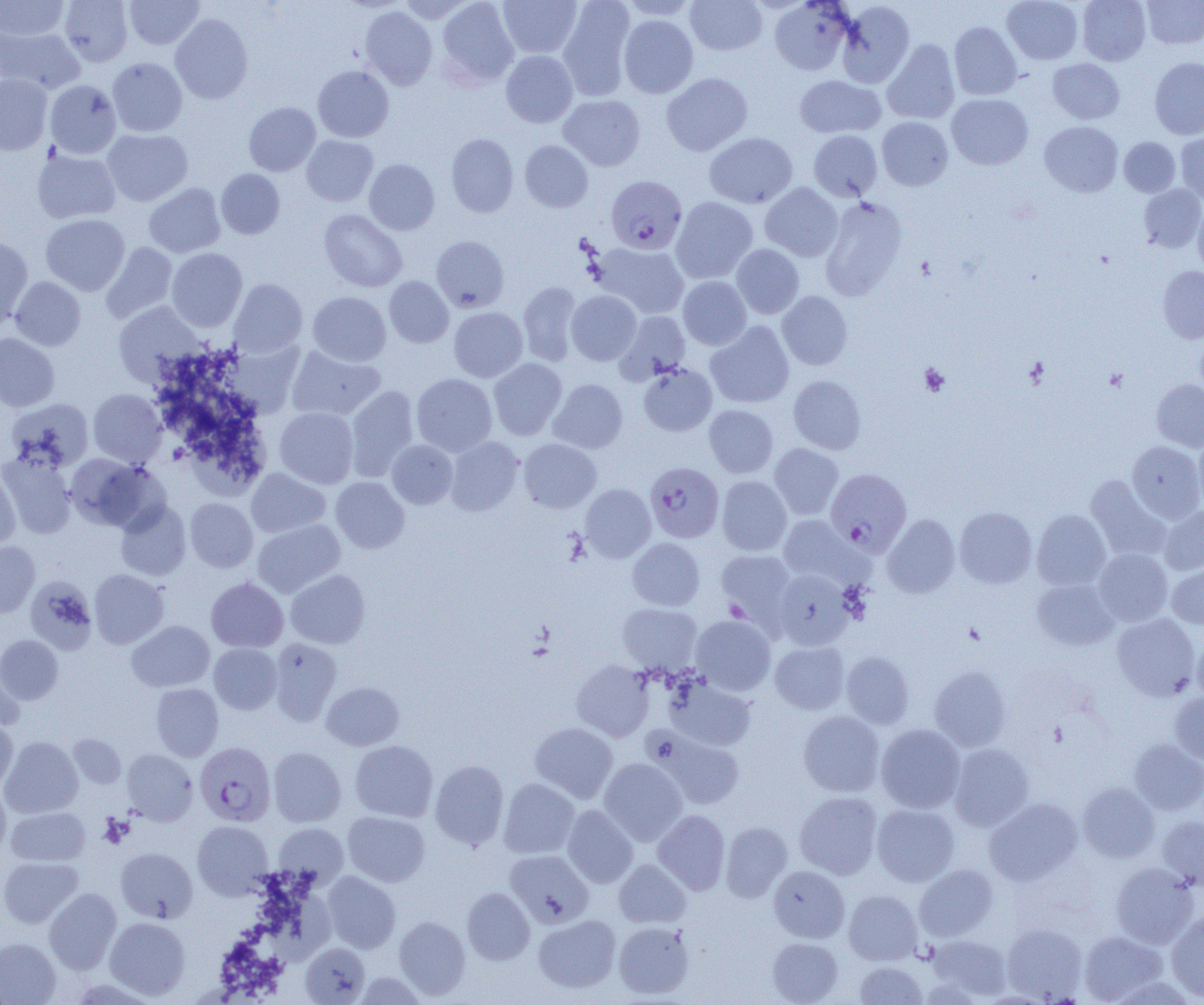

Approximate bounding boxes as named x1/y1/x2/y2 corners in pixels. Platelet locations: (x1=919, y1=363, x2=950, y2=396), (x1=99, y1=815, x2=133, y2=847). Plasmodium falciparum-infected red blood cell locations (subset): (x1=645, y1=461, x2=724, y2=543), (x1=826, y1=469, x2=911, y2=555), (x1=195, y1=742, x2=276, y2=826). Uninfected red blood cell locations (subset): (x1=0, y1=0, x2=69, y2=40), (x1=59, y1=0, x2=133, y2=66), (x1=125, y1=0, x2=204, y2=49), (x1=436, y1=0, x2=518, y2=88), (x1=498, y1=0, x2=582, y2=58), (x1=685, y1=0, x2=767, y2=55), (x1=1002, y1=0, x2=1083, y2=65), (x1=1078, y1=0, x2=1151, y2=65), (x1=1141, y1=0, x2=1204, y2=49), (x1=557, y1=1, x2=636, y2=100), (x1=619, y1=1, x2=699, y2=21), (x1=769, y1=1, x2=853, y2=75), (x1=836, y1=1, x2=915, y2=88), (x1=360, y1=6, x2=437, y2=90), (x1=170, y1=14, x2=253, y2=104), (x1=619, y1=15, x2=698, y2=98), (x1=949, y1=21, x2=1021, y2=100), (x1=0, y1=27, x2=85, y2=93), (x1=882, y1=39, x2=960, y2=125), (x1=501, y1=50, x2=578, y2=128), (x1=107, y1=58, x2=187, y2=136), (x1=1048, y1=58, x2=1125, y2=124), (x1=1149, y1=58, x2=1204, y2=139), (x1=312, y1=65, x2=394, y2=143), (x1=661, y1=73, x2=752, y2=156), (x1=0, y1=75, x2=52, y2=155), (x1=795, y1=75, x2=885, y2=138), (x1=45, y1=80, x2=121, y2=159), (x1=946, y1=93, x2=1033, y2=169), (x1=559, y1=94, x2=645, y2=171), (x1=244, y1=102, x2=321, y2=176), (x1=877, y1=116, x2=953, y2=190), (x1=1040, y1=121, x2=1123, y2=197), (x1=102, y1=129, x2=193, y2=206), (x1=808, y1=130, x2=883, y2=201), (x1=704, y1=132, x2=797, y2=208), (x1=446, y1=133, x2=518, y2=217), (x1=1176, y1=134, x2=1203, y2=203), (x1=301, y1=135, x2=378, y2=206), (x1=1119, y1=137, x2=1180, y2=197), (x1=520, y1=140, x2=593, y2=212), (x1=32, y1=148, x2=121, y2=224), (x1=364, y1=159, x2=439, y2=234), (x1=216, y1=168, x2=285, y2=239), (x1=144, y1=183, x2=225, y2=257), (x1=760, y1=183, x2=843, y2=261), (x1=1138, y1=184, x2=1204, y2=253), (x1=671, y1=197, x2=758, y2=283), (x1=820, y1=197, x2=907, y2=299), (x1=1193, y1=202, x2=1204, y2=275), (x1=319, y1=209, x2=407, y2=292), (x1=41, y1=214, x2=130, y2=295), (x1=0, y1=236, x2=33, y2=330), (x1=432, y1=236, x2=509, y2=312), (x1=100, y1=242, x2=178, y2=323), (x1=596, y1=243, x2=689, y2=318), (x1=731, y1=244, x2=804, y2=319), (x1=167, y1=248, x2=247, y2=331), (x1=1158, y1=266, x2=1204, y2=343), (x1=385, y1=276, x2=454, y2=347), (x1=678, y1=276, x2=752, y2=350), (x1=10, y1=277, x2=85, y2=351), (x1=229, y1=279, x2=307, y2=358), (x1=518, y1=281, x2=582, y2=366), (x1=566, y1=290, x2=641, y2=365), (x1=777, y1=291, x2=853, y2=370), (x1=308, y1=292, x2=391, y2=366), (x1=113, y1=302, x2=203, y2=385), (x1=449, y1=307, x2=528, y2=382), (x1=616, y1=311, x2=690, y2=382), (x1=706, y1=321, x2=794, y2=408), (x1=1195, y1=332, x2=1204, y2=402), (x1=0, y1=333, x2=60, y2=412), (x1=221, y1=340, x2=305, y2=418), (x1=286, y1=347, x2=384, y2=421), (x1=488, y1=358, x2=567, y2=440), (x1=638, y1=363, x2=717, y2=436), (x1=411, y1=373, x2=497, y2=456), (x1=788, y1=376, x2=866, y2=454), (x1=1151, y1=378, x2=1204, y2=452), (x1=548, y1=379, x2=628, y2=454), (x1=346, y1=385, x2=419, y2=481), (x1=88, y1=389, x2=166, y2=466), (x1=6, y1=399, x2=93, y2=472), (x1=704, y1=405, x2=778, y2=477), (x1=275, y1=407, x2=358, y2=488), (x1=1193, y1=431, x2=1204, y2=511), (x1=445, y1=436, x2=524, y2=516), (x1=519, y1=438, x2=601, y2=513), (x1=387, y1=440, x2=457, y2=508), (x1=1127, y1=440, x2=1204, y2=522), (x1=769, y1=443, x2=843, y2=520), (x1=1, y1=452, x2=77, y2=539), (x1=66, y1=454, x2=166, y2=532), (x1=246, y1=468, x2=330, y2=538), (x1=0, y1=470, x2=20, y2=548), (x1=1085, y1=475, x2=1172, y2=561), (x1=717, y1=476, x2=792, y2=555), (x1=331, y1=477, x2=409, y2=553), (x1=580, y1=484, x2=655, y2=562), (x1=185, y1=498, x2=258, y2=572), (x1=115, y1=501, x2=191, y2=581), (x1=1158, y1=505, x2=1204, y2=575), (x1=955, y1=506, x2=1037, y2=588), (x1=1032, y1=509, x2=1111, y2=590), (x1=882, y1=514, x2=960, y2=598), (x1=778, y1=515, x2=862, y2=586), (x1=252, y1=519, x2=345, y2=597), (x1=627, y1=538, x2=705, y2=610), (x1=0, y1=541, x2=40, y2=618), (x1=1093, y1=548, x2=1173, y2=626), (x1=716, y1=549, x2=796, y2=627), (x1=1166, y1=561, x2=1204, y2=628), (x1=89, y1=569, x2=168, y2=648), (x1=773, y1=569, x2=854, y2=650), (x1=286, y1=570, x2=370, y2=648), (x1=25, y1=576, x2=98, y2=654), (x1=206, y1=577, x2=288, y2=652), (x1=1032, y1=578, x2=1118, y2=651), (x1=618, y1=603, x2=702, y2=674), (x1=1111, y1=613, x2=1200, y2=700), (x1=691, y1=615, x2=776, y2=695), (x1=126, y1=620, x2=215, y2=692), (x1=0, y1=635, x2=63, y2=704), (x1=1193, y1=635, x2=1204, y2=705), (x1=269, y1=638, x2=342, y2=725), (x1=770, y1=641, x2=849, y2=714), (x1=209, y1=643, x2=282, y2=714), (x1=841, y1=651, x2=914, y2=729), (x1=0, y1=656, x2=25, y2=732), (x1=571, y1=660, x2=654, y2=742), (x1=929, y1=665, x2=1012, y2=751), (x1=665, y1=677, x2=756, y2=751), (x1=322, y1=682, x2=404, y2=750), (x1=151, y1=683, x2=224, y2=761), (x1=1169, y1=690, x2=1204, y2=764), (x1=798, y1=710, x2=885, y2=797), (x1=0, y1=719, x2=18, y2=791), (x1=530, y1=722, x2=618, y2=803), (x1=876, y1=724, x2=965, y2=813), (x1=648, y1=729, x2=746, y2=809), (x1=68, y1=734, x2=126, y2=789), (x1=1, y1=737, x2=83, y2=818), (x1=1129, y1=739, x2=1204, y2=815), (x1=350, y1=740, x2=438, y2=822), (x1=949, y1=743, x2=1034, y2=831), (x1=268, y1=747, x2=347, y2=827), (x1=122, y1=749, x2=197, y2=824), (x1=599, y1=758, x2=688, y2=845), (x1=430, y1=759, x2=509, y2=850), (x1=498, y1=778, x2=579, y2=858), (x1=1078, y1=782, x2=1159, y2=863), (x1=0, y1=784, x2=11, y2=858), (x1=794, y1=791, x2=882, y2=880), (x1=985, y1=797, x2=1083, y2=885), (x1=872, y1=803, x2=960, y2=886), (x1=562, y1=805, x2=639, y2=888), (x1=6, y1=807, x2=90, y2=866), (x1=652, y1=810, x2=730, y2=895), (x1=343, y1=811, x2=430, y2=886), (x1=1157, y1=815, x2=1204, y2=890), (x1=192, y1=820, x2=274, y2=899), (x1=720, y1=821, x2=792, y2=901), (x1=274, y1=823, x2=348, y2=887), (x1=115, y1=847, x2=198, y2=923), (x1=505, y1=850, x2=594, y2=927), (x1=0, y1=856, x2=83, y2=928), (x1=614, y1=859, x2=691, y2=928), (x1=1110, y1=862, x2=1198, y2=949), (x1=915, y1=864, x2=998, y2=941), (x1=769, y1=865, x2=850, y2=942), (x1=322, y1=871, x2=400, y2=953), (x1=268, y1=885, x2=332, y2=968), (x1=461, y1=887, x2=535, y2=965), (x1=44, y1=888, x2=122, y2=974), (x1=843, y1=889, x2=922, y2=965), (x1=1166, y1=911, x2=1204, y2=1002), (x1=533, y1=914, x2=621, y2=993), (x1=394, y1=916, x2=471, y2=999), (x1=104, y1=917, x2=191, y2=1000), (x1=613, y1=921, x2=694, y2=999), (x1=1001, y1=921, x2=1087, y2=1002), (x1=1079, y1=930, x2=1167, y2=1003), (x1=928, y1=934, x2=1012, y2=1000), (x1=0, y1=937, x2=60, y2=1005), (x1=767, y1=938, x2=843, y2=1004), (x1=300, y1=942, x2=370, y2=1004), (x1=854, y1=961, x2=927, y2=1005), (x1=352, y1=971, x2=428, y2=1004). Slide-level diagnosis: Plasmodium falciparum. Image is 1204×1005 pixels. Light microscopy. Thin blood smear. One field of a larger specimen. 1000x magnification.